Describe the morphology of the red blood cells.
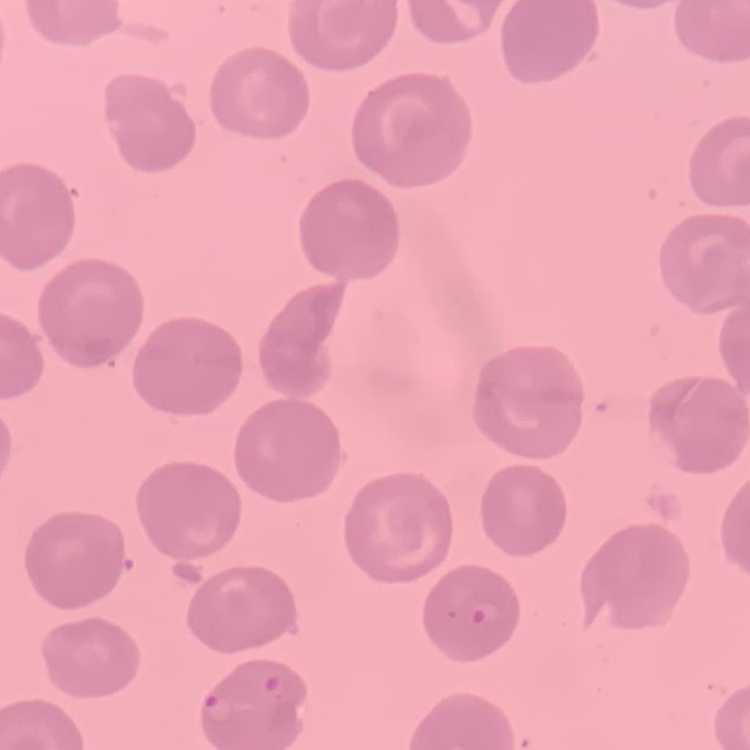

They show no rouleaux formation.

stain: Field's or Giemsa
image_type: square crop of a larger photomicrograph
preparation: thin peripheral smear